Assess the morphology of the erythrocytes.
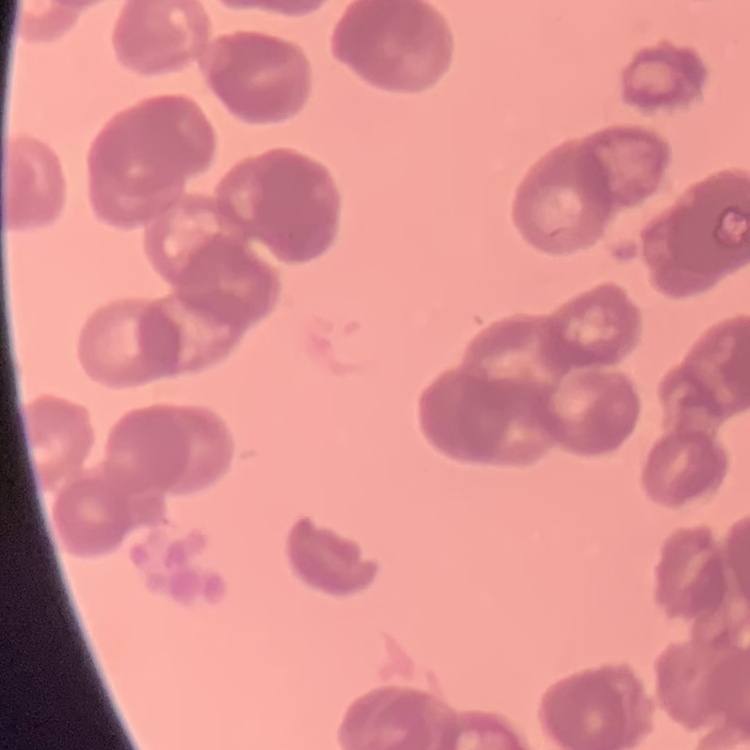
Rouleaux formation.

Square crop of a larger photomicrograph. Thin blood film. Field's or Giemsa stain.